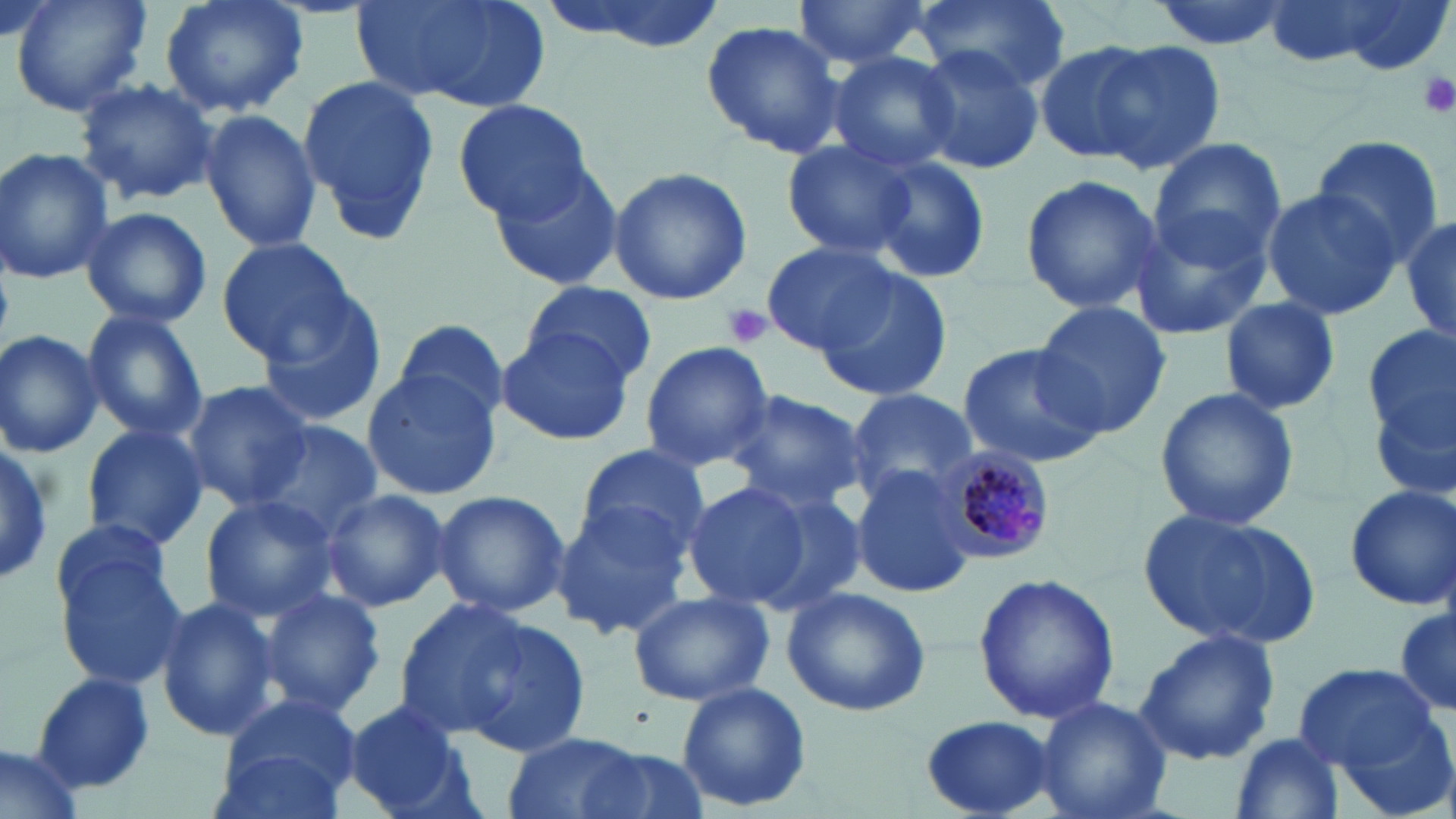
slide_level_diagnosis: Plasmodium malariae
stain: May-Grünwald-Giemsa
plasmodium_malariae_infected_red_blood_cell_locations: 'approximate bounding boxes as named x1/y1/x2/y2 corners in pixels: (x1=933, y1=446, x2=1056, y2=564)'
platelet_locations: 'approximate bounding boxes as named x1/y1/x2/y2 corners in pixels: (x1=1416, y1=69, x2=1452, y2=120), (x1=720, y1=301, x2=774, y2=349)'
image_size: 1456×819 pixels
uninfected_red_blood_cell_locations: 'approximate bounding boxes as named x1/y1/x2/y2 corners in pixels: (x1=10, y1=0, x2=152, y2=119), (x1=158, y1=0, x2=307, y2=119), (x1=350, y1=0, x2=553, y2=113), (x1=533, y1=0, x2=732, y2=55), (x1=791, y1=0, x2=936, y2=69), (x1=915, y1=0, x2=1070, y2=94), (x1=1311, y1=1, x2=1454, y2=73), (x1=699, y1=19, x2=847, y2=159), (x1=1087, y1=39, x2=1227, y2=176), (x1=1036, y1=40, x2=1160, y2=165), (x1=909, y1=42, x2=1043, y2=179), (x1=827, y1=51, x2=959, y2=173), (x1=295, y1=72, x2=440, y2=245), (x1=75, y1=77, x2=221, y2=207), (x1=452, y1=99, x2=594, y2=222), (x1=199, y1=109, x2=322, y2=253), (x1=1146, y1=137, x2=1285, y2=276), (x1=1308, y1=138, x2=1444, y2=262), (x1=780, y1=139, x2=919, y2=260), (x1=0, y1=148, x2=116, y2=286), (x1=867, y1=156, x2=992, y2=283), (x1=487, y1=163, x2=627, y2=294), (x1=608, y1=166, x2=752, y2=305), (x1=1019, y1=171, x2=1162, y2=316), (x1=1260, y1=189, x2=1403, y2=319), (x1=1127, y1=203, x2=1275, y2=343), (x1=79, y1=206, x2=213, y2=328), (x1=1401, y1=208, x2=1456, y2=353), (x1=213, y1=238, x2=359, y2=364), (x1=761, y1=242, x2=898, y2=354), (x1=808, y1=266, x2=955, y2=403), (x1=523, y1=281, x2=656, y2=385), (x1=257, y1=294, x2=388, y2=430), (x1=1218, y1=297, x2=1342, y2=416), (x1=1030, y1=301, x2=1174, y2=437), (x1=81, y1=307, x2=211, y2=445), (x1=392, y1=318, x2=510, y2=424), (x1=495, y1=324, x2=633, y2=445), (x1=1363, y1=329, x2=1455, y2=496), (x1=0, y1=330, x2=104, y2=459), (x1=640, y1=341, x2=774, y2=471), (x1=955, y1=341, x2=1108, y2=467), (x1=361, y1=369, x2=502, y2=500), (x1=180, y1=380, x2=313, y2=509), (x1=1154, y1=386, x2=1300, y2=531), (x1=722, y1=389, x2=866, y2=517), (x1=840, y1=389, x2=979, y2=502), (x1=78, y1=423, x2=210, y2=552), (x1=250, y1=424, x2=381, y2=541), (x1=0, y1=442, x2=57, y2=586), (x1=574, y1=443, x2=709, y2=561), (x1=850, y1=463, x2=977, y2=598), (x1=681, y1=479, x2=821, y2=614), (x1=1342, y1=482, x2=1456, y2=611), (x1=745, y1=486, x2=872, y2=616), (x1=319, y1=487, x2=451, y2=612), (x1=432, y1=489, x2=568, y2=617), (x1=198, y1=494, x2=341, y2=622), (x1=548, y1=498, x2=698, y2=640), (x1=1138, y1=507, x2=1320, y2=653), (x1=48, y1=531, x2=188, y2=692), (x1=974, y1=571, x2=1119, y2=724), (x1=782, y1=587, x2=932, y2=719), (x1=256, y1=588, x2=386, y2=719), (x1=627, y1=591, x2=773, y2=707), (x1=154, y1=594, x2=277, y2=743), (x1=391, y1=597, x2=542, y2=739), (x1=1394, y1=603, x2=1455, y2=717), (x1=448, y1=613, x2=594, y2=761), (x1=1133, y1=630, x2=1281, y2=765), (x1=1294, y1=661, x2=1437, y2=776), (x1=32, y1=672, x2=155, y2=795), (x1=677, y1=681, x2=812, y2=814), (x1=213, y1=692, x2=365, y2=813), (x1=1034, y1=695, x2=1172, y2=819), (x1=341, y1=699, x2=470, y2=816), (x1=1329, y1=709, x2=1456, y2=819), (x1=920, y1=713, x2=1058, y2=818), (x1=1229, y1=731, x2=1347, y2=818), (x1=501, y1=732, x2=653, y2=819), (x1=0, y1=741, x2=87, y2=819), (x1=565, y1=745, x2=710, y2=819)'
magnification: 1000x
field_of_view: single
modality: light microscopy
preparation: thin blood smear